Give the extent of all uninfected red blood cells.
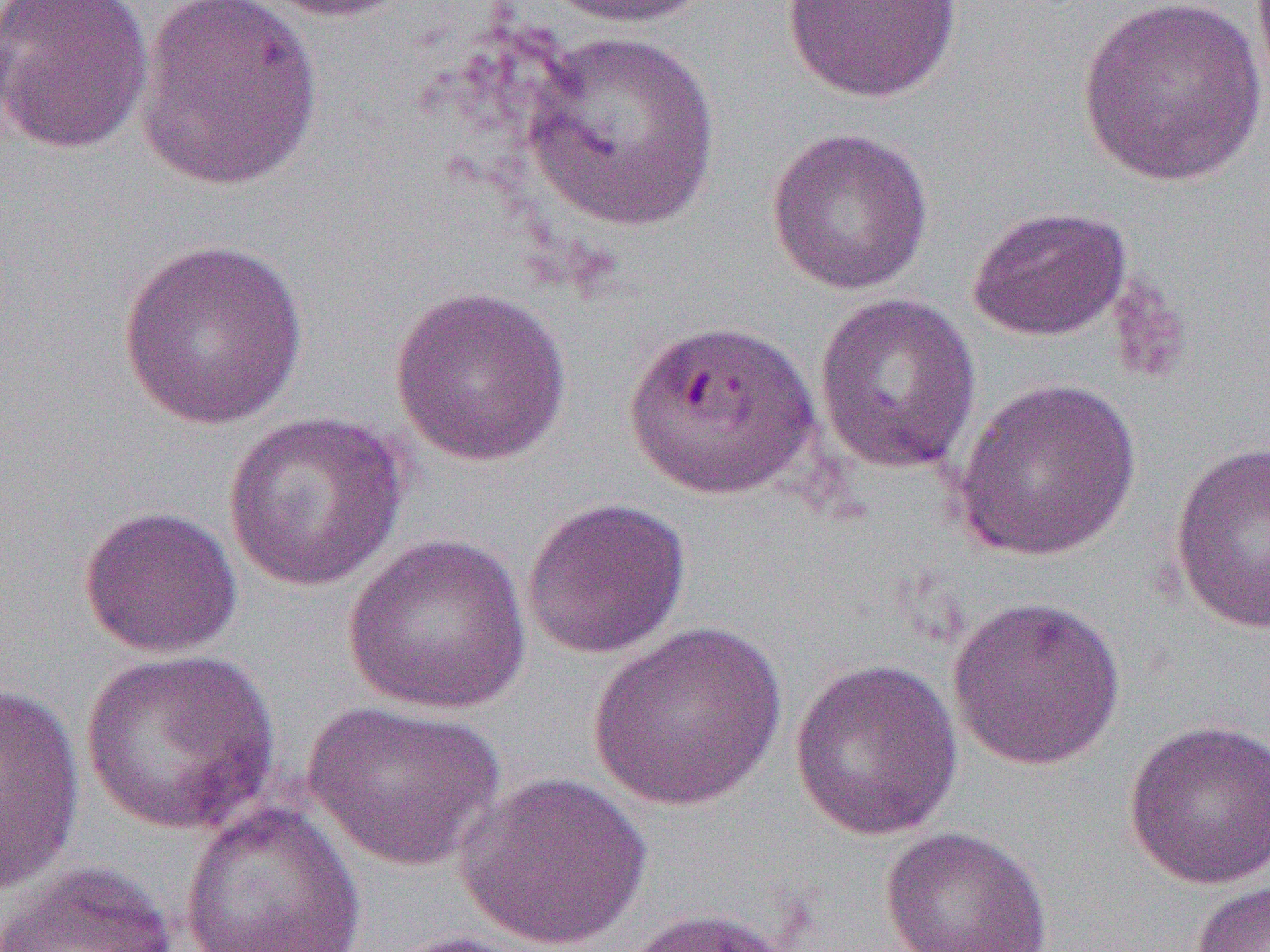
Approximate bounding boxes as (x1,y1)-(x2,y2) corner pairs in pixels.
Uninfected red blood cells: (1,0)-(154,155), (246,0)-(417,23), (538,0)-(716,30), (1075,0)-(1268,187), (134,1)-(324,192), (780,1)-(963,103), (522,30)-(722,232), (766,127)-(934,296), (966,205)-(1133,342), (117,237)-(311,430), (389,285)-(572,468), (813,292)-(982,476), (952,376)-(1142,563), (221,410)-(410,593), (1168,440)-(1270,636), (521,496)-(691,660), (78,505)-(243,658), (341,533)-(532,715), (946,595)-(1126,771), (588,621)-(789,811), (80,648)-(282,834), (788,657)-(964,841), (0,681)-(85,893), (301,700)-(506,871), (1122,718)-(1270,891), (455,771)-(652,952), (178,801)-(368,952), (879,825)-(1053,952), (2,861)-(179,952), (1187,878)-(1270,952), (620,906)-(802,952), (382,930)-(547,952).

slide-level diagnosis = Plasmodium falciparum
image size = 1270×952 pixels
modality = light microscopy
preparation = thin blood film
field of view = one of a larger specimen
magnification = 1000x